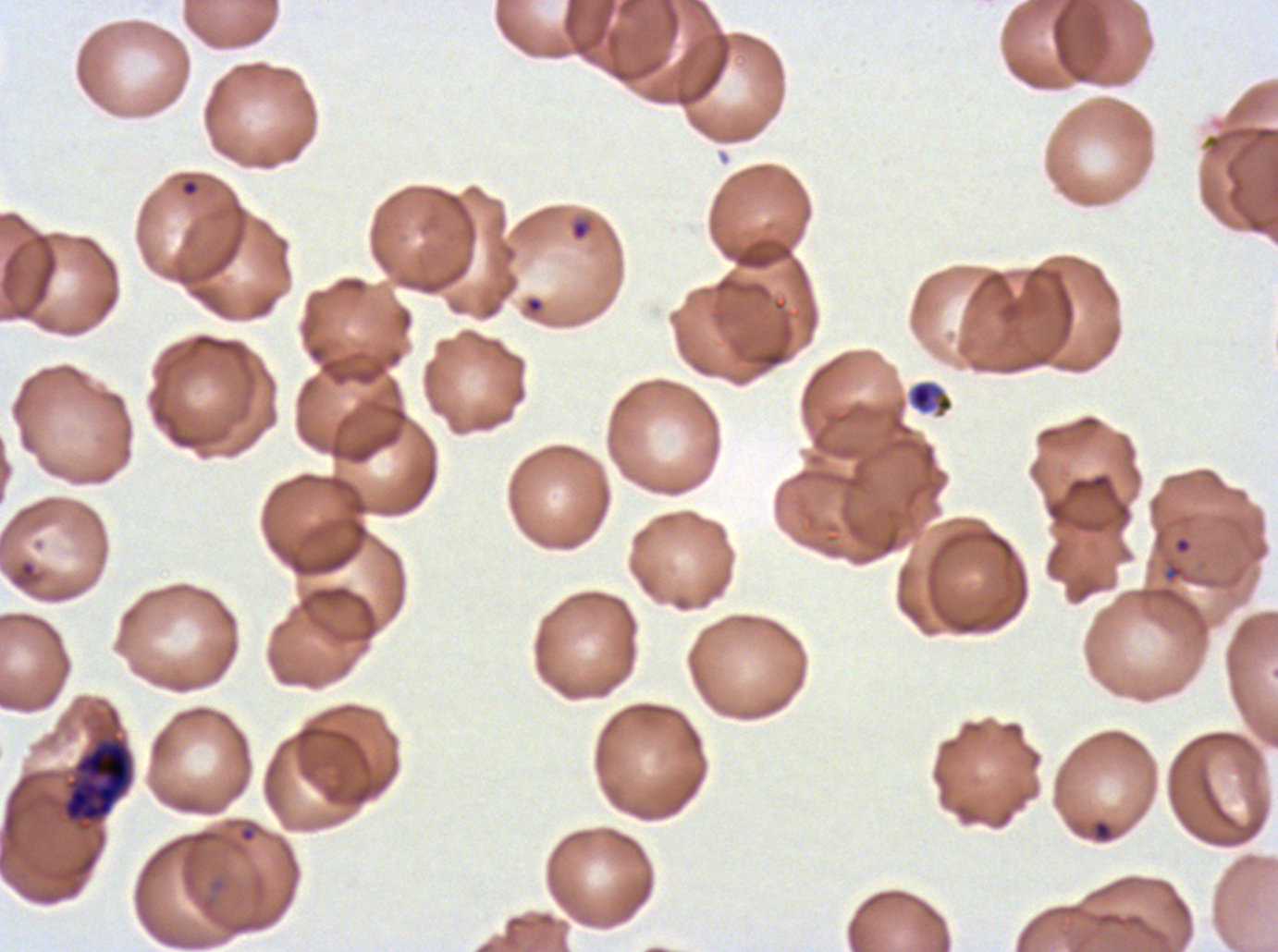

notation = approximate bounding boxes as {x1, y1, x2, y2} in pixels
late schizont locations = {57, 727, 136, 834}
ring locations = {180, 178, 200, 197}, {570, 217, 594, 242}, {1173, 535, 1193, 555}, {238, 824, 257, 844}
debris locations = {906, 379, 954, 419}, {1092, 819, 1113, 843}
life-cycle stages observed = ring, late schizont
field of view = sub-image separated from a larger composite
specimen = Plasmodium falciparum from a patient in The Gambia, cultured ex vivo for 24 to 48 hours
image size = 1278×952 pixels
stain = Giemsa
preparation = thin blood smear